Locate every blood parasite and identify its species.
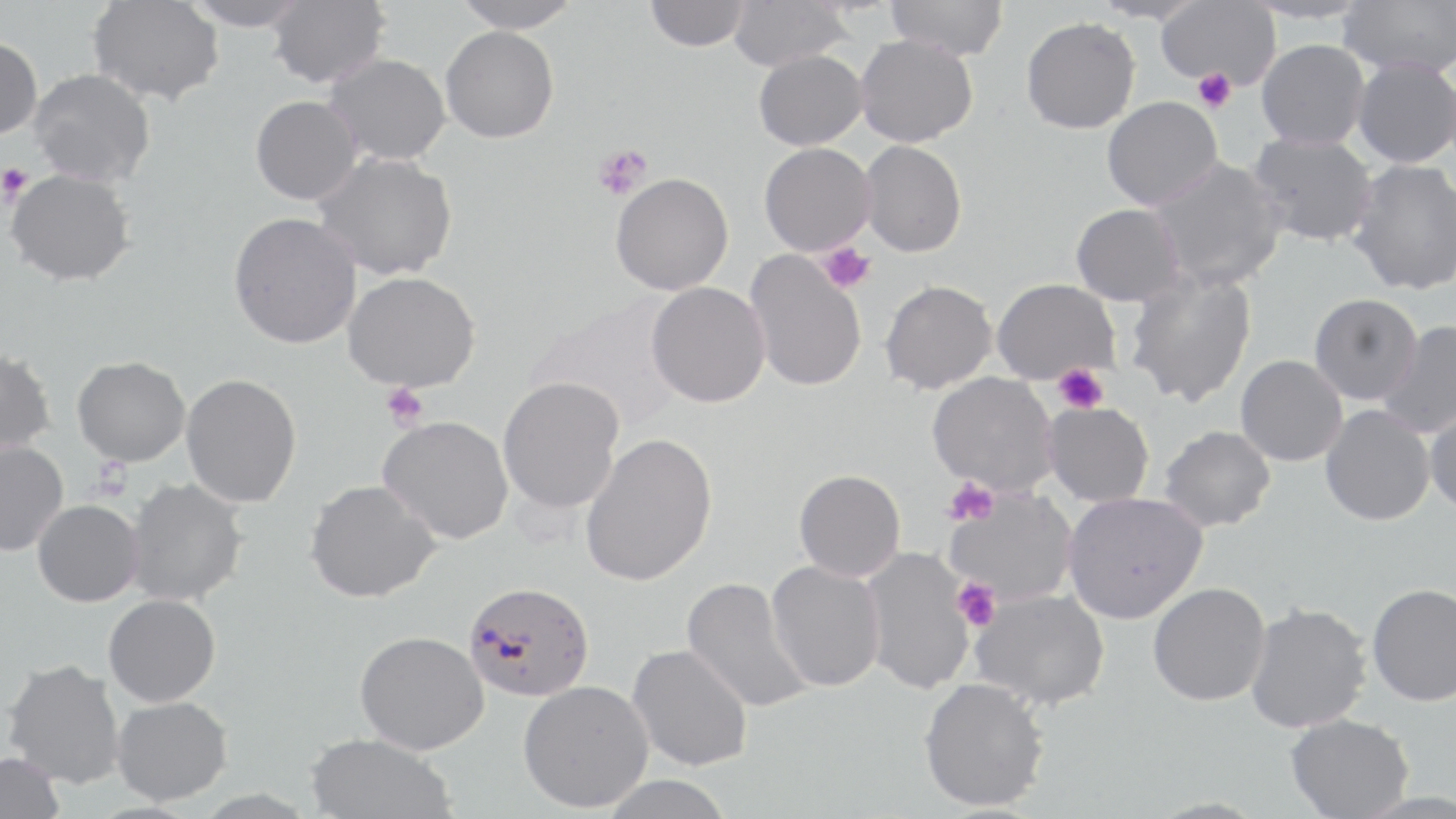
Approximate bounding boxes as [x1, y1, x2, y2] in pixels.
Plasmodium falciparum-infected red blood cells: [462, 580, 595, 701].
No Plasmodium ovale, Plasmodium malariae, Plasmodium vivax, Babesia divergens, or Trypanosoma brucei observed.

slide-level diagnosis = Plasmodium falciparum
uninfected red blood cell locations = approximate bounding boxes as [x1, y1, x2, y2] in pixels: [88, 0, 224, 105], [183, 0, 310, 31], [267, 0, 390, 88], [450, 0, 583, 33], [644, 0, 751, 52], [728, 0, 851, 71], [886, 0, 1008, 61], [1090, 0, 1207, 25], [1156, 0, 1281, 89], [1338, 0, 1456, 77], [1021, 16, 1141, 134], [440, 25, 559, 143], [855, 34, 978, 147], [0, 36, 43, 140], [1256, 39, 1370, 150], [752, 49, 867, 150], [324, 53, 450, 166], [1352, 57, 1456, 169], [27, 68, 156, 187], [250, 95, 362, 205], [1101, 96, 1224, 211], [1247, 132, 1378, 247], [859, 140, 967, 257], [759, 142, 876, 256], [313, 152, 457, 281], [1147, 157, 1287, 291], [1348, 158, 1456, 296], [5, 168, 136, 286], [610, 172, 733, 295], [1070, 203, 1186, 306], [228, 211, 362, 349], [744, 251, 866, 392], [1124, 270, 1257, 406], [342, 271, 480, 391], [991, 278, 1120, 384], [880, 280, 997, 394], [646, 282, 770, 408], [1308, 293, 1422, 404], [527, 296, 685, 432], [1378, 320, 1456, 438], [0, 347, 56, 456], [1235, 355, 1348, 466], [72, 356, 190, 466], [927, 372, 1058, 495], [181, 373, 302, 508], [498, 376, 624, 514], [1043, 402, 1154, 507], [1320, 404, 1435, 526], [1424, 406, 1456, 517], [377, 415, 513, 544], [1158, 425, 1276, 532], [580, 432, 717, 587], [0, 440, 69, 557], [793, 469, 906, 582], [125, 477, 247, 607], [304, 479, 440, 603], [945, 489, 1077, 605], [1062, 492, 1206, 624], [32, 499, 143, 606], [860, 547, 976, 695], [765, 560, 885, 693], [682, 576, 813, 714], [1147, 582, 1270, 706], [1366, 582, 1456, 706], [970, 589, 1109, 710], [103, 594, 221, 707], [1244, 602, 1372, 733], [354, 630, 489, 755], [627, 644, 753, 772], [3, 658, 126, 788], [918, 677, 1050, 812], [518, 680, 654, 812], [111, 696, 232, 805], [1284, 713, 1414, 819], [305, 732, 458, 819], [0, 751, 65, 819], [598, 775, 736, 819]
magnification = 1000x
stain = May-Grünwald-Giemsa
field of view = one of a larger specimen
image size = 1456×819 pixels
platelet locations = approximate bounding boxes as [x1, y1, x2, y2] in pixels: [1193, 68, 1236, 112], [593, 144, 651, 201], [0, 164, 32, 202], [818, 243, 875, 295], [1053, 364, 1108, 413], [381, 383, 429, 430], [944, 478, 1000, 526], [953, 578, 1001, 631]
preparation = thin blood film
modality = light microscopy